Locate every Plasmodium vivax-infected red blood cell.
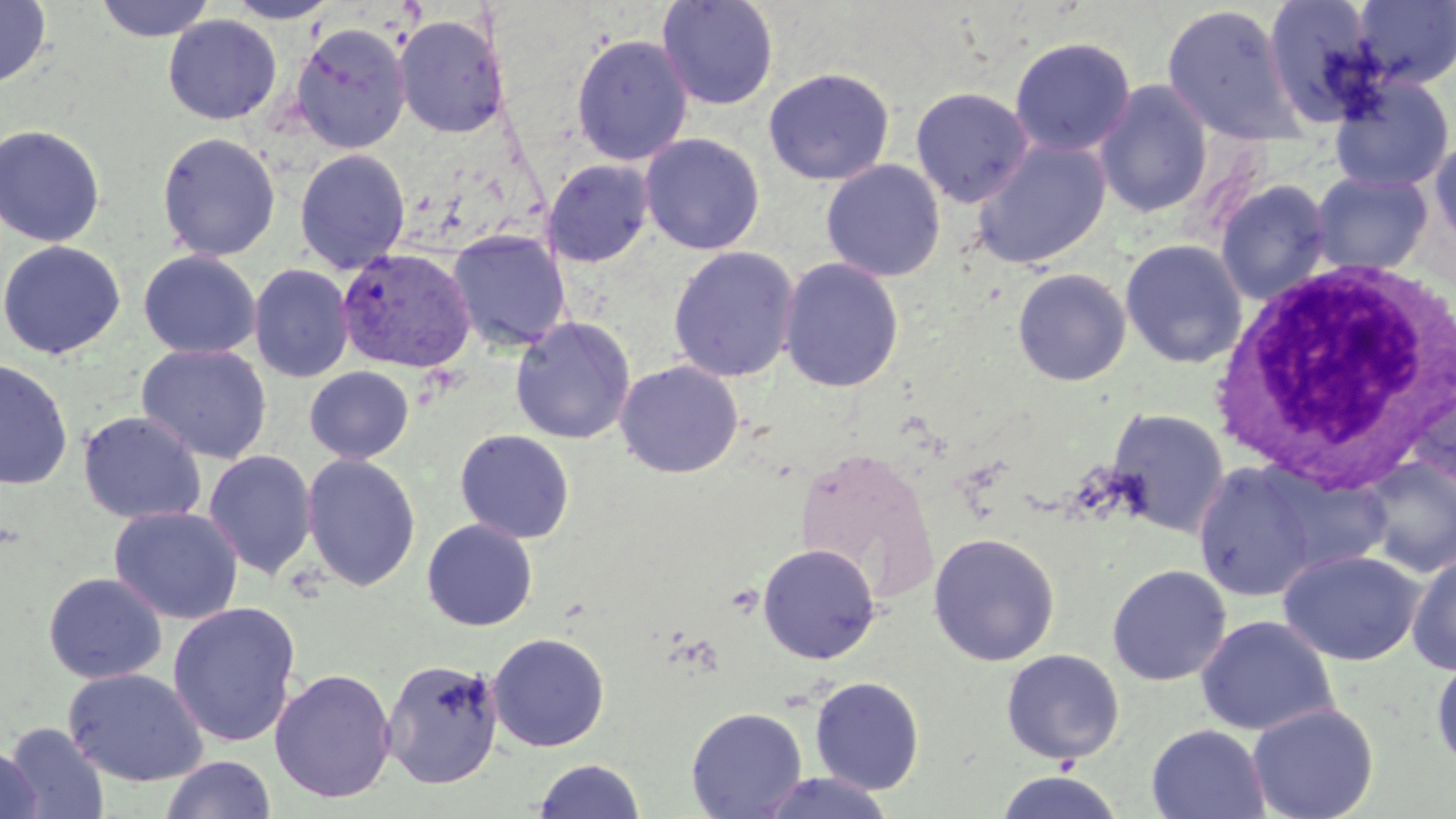
Approximate bounding boxes as named x1/y1/x2/y2 corners in pixels.
Plasmodium vivax-infected red blood cells: (x1=337, y1=247, x2=476, y2=374).

slide_level_diagnosis: Plasmodium vivax
image_size: 1456×819 pixels
modality: light microscopy
white_blood_cell_locations: 'approximate bounding boxes as named x1/y1/x2/y2 corners in pixels: (x1=1212, y1=257, x2=1456, y2=492)'
magnification: 1000x
uninfected_red_blood_cell_locations: 'approximate bounding boxes as named x1/y1/x2/y2 corners in pixels: (x1=0, y1=0, x2=52, y2=89), (x1=94, y1=0, x2=218, y2=43), (x1=656, y1=0, x2=780, y2=111), (x1=224, y1=1, x2=341, y2=24), (x1=1262, y1=1, x2=1381, y2=128), (x1=1351, y1=1, x2=1456, y2=88), (x1=1161, y1=3, x2=1304, y2=148), (x1=393, y1=14, x2=510, y2=138), (x1=163, y1=15, x2=282, y2=125), (x1=290, y1=23, x2=411, y2=154), (x1=571, y1=33, x2=693, y2=166), (x1=1009, y1=36, x2=1136, y2=157), (x1=763, y1=67, x2=895, y2=186), (x1=1329, y1=74, x2=1454, y2=194), (x1=1093, y1=80, x2=1213, y2=219), (x1=910, y1=87, x2=1033, y2=208), (x1=0, y1=124, x2=106, y2=248), (x1=1428, y1=131, x2=1456, y2=254), (x1=157, y1=132, x2=281, y2=261), (x1=640, y1=134, x2=765, y2=255), (x1=971, y1=138, x2=1112, y2=270), (x1=294, y1=149, x2=411, y2=274), (x1=821, y1=159, x2=946, y2=282), (x1=543, y1=160, x2=654, y2=268), (x1=1309, y1=171, x2=1434, y2=275), (x1=1214, y1=179, x2=1331, y2=306), (x1=447, y1=230, x2=571, y2=351), (x1=1120, y1=239, x2=1248, y2=368), (x1=0, y1=240, x2=125, y2=360), (x1=667, y1=245, x2=800, y2=382), (x1=138, y1=250, x2=260, y2=359), (x1=778, y1=257, x2=904, y2=393), (x1=249, y1=264, x2=354, y2=383), (x1=1012, y1=268, x2=1132, y2=386), (x1=510, y1=316, x2=635, y2=445), (x1=136, y1=344, x2=272, y2=464), (x1=0, y1=358, x2=74, y2=491), (x1=614, y1=360, x2=744, y2=479), (x1=304, y1=366, x2=414, y2=464), (x1=1408, y1=374, x2=1456, y2=500), (x1=1106, y1=408, x2=1229, y2=538), (x1=78, y1=411, x2=207, y2=524), (x1=455, y1=428, x2=575, y2=544), (x1=204, y1=450, x2=317, y2=579), (x1=301, y1=453, x2=421, y2=592), (x1=1357, y1=457, x2=1456, y2=578), (x1=1192, y1=461, x2=1322, y2=602), (x1=109, y1=506, x2=244, y2=625), (x1=422, y1=519, x2=538, y2=631), (x1=928, y1=533, x2=1060, y2=666), (x1=757, y1=543, x2=881, y2=664), (x1=1278, y1=549, x2=1425, y2=666), (x1=1407, y1=551, x2=1456, y2=674), (x1=1107, y1=564, x2=1231, y2=686), (x1=43, y1=572, x2=167, y2=684), (x1=167, y1=602, x2=301, y2=747), (x1=1196, y1=615, x2=1338, y2=737), (x1=487, y1=632, x2=610, y2=752), (x1=1001, y1=649, x2=1125, y2=764), (x1=1431, y1=655, x2=1456, y2=770), (x1=382, y1=658, x2=504, y2=789), (x1=62, y1=667, x2=209, y2=788), (x1=269, y1=668, x2=397, y2=803), (x1=810, y1=676, x2=925, y2=795), (x1=1247, y1=703, x2=1379, y2=819), (x1=686, y1=707, x2=808, y2=818), (x1=3, y1=722, x2=109, y2=819), (x1=1146, y1=724, x2=1270, y2=819), (x1=0, y1=745, x2=41, y2=819), (x1=161, y1=755, x2=276, y2=819), (x1=533, y1=758, x2=646, y2=818), (x1=995, y1=770, x2=1125, y2=818), (x1=755, y1=771, x2=895, y2=818)'
preparation: thin blood film
stain: May-Grünwald-Giemsa
field_of_view: single